Mark where platelets are.
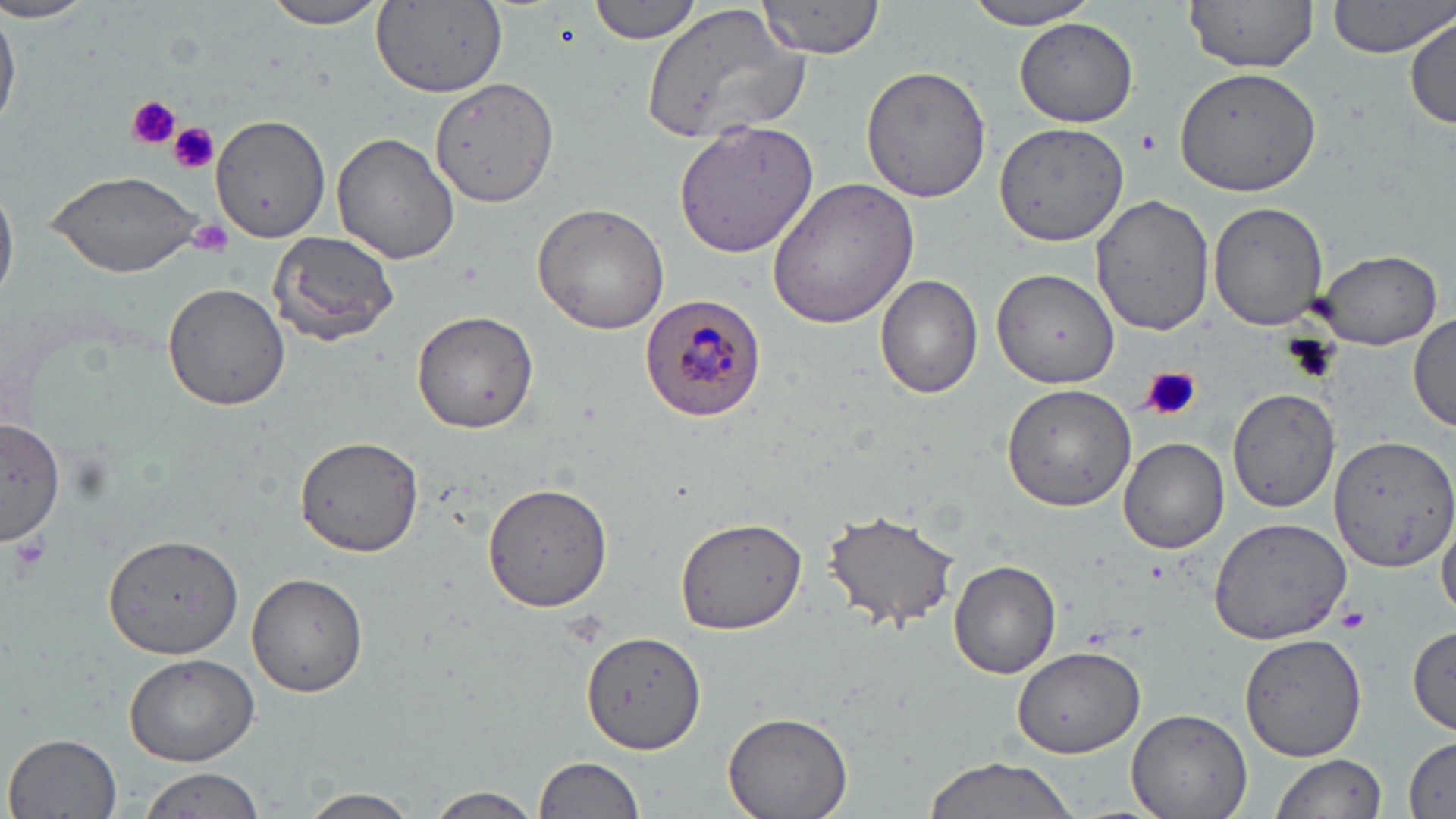
Approximate bounding boxes as named x1/y1/x2/y2 corners in pixels.
Platelets: (x1=124, y1=95, x2=180, y2=151), (x1=169, y1=122, x2=220, y2=174), (x1=1135, y1=128, x2=1162, y2=154), (x1=187, y1=217, x2=235, y2=256), (x1=1141, y1=366, x2=1201, y2=423), (x1=5, y1=534, x2=50, y2=584), (x1=1336, y1=604, x2=1371, y2=635).

{
  "slide_level_diagnosis": "Plasmodium malariae",
  "magnification": "1000x",
  "modality": "light microscopy",
  "preparation": "thin blood smear",
  "image_size": "1456×819 pixels",
  "uninfected_red_blood_cell_locations": "approximate bounding boxes as named x1/y1/x2/y2 corners in pixels: (x1=588, y1=0, x2=705, y2=44), (x1=1184, y1=0, x2=1320, y2=71), (x1=1327, y1=0, x2=1455, y2=59), (x1=963, y1=1, x2=1105, y2=28), (x1=0, y1=2, x2=98, y2=25), (x1=257, y1=2, x2=394, y2=29), (x1=373, y1=2, x2=510, y2=97), (x1=756, y1=2, x2=887, y2=58), (x1=0, y1=3, x2=19, y2=134), (x1=642, y1=4, x2=811, y2=145), (x1=1408, y1=13, x2=1455, y2=130), (x1=1014, y1=17, x2=1139, y2=127), (x1=860, y1=63, x2=991, y2=203), (x1=1172, y1=64, x2=1323, y2=196), (x1=432, y1=76, x2=559, y2=208), (x1=210, y1=112, x2=331, y2=243), (x1=674, y1=116, x2=821, y2=259), (x1=996, y1=120, x2=1131, y2=251), (x1=330, y1=131, x2=462, y2=265), (x1=45, y1=169, x2=206, y2=277), (x1=765, y1=176, x2=922, y2=330), (x1=0, y1=178, x2=18, y2=307), (x1=290, y1=183, x2=439, y2=335), (x1=1092, y1=194, x2=1215, y2=335), (x1=1208, y1=201, x2=1329, y2=330), (x1=531, y1=203, x2=670, y2=335), (x1=268, y1=230, x2=402, y2=346), (x1=1312, y1=248, x2=1442, y2=350), (x1=991, y1=267, x2=1119, y2=390), (x1=876, y1=275, x2=984, y2=400), (x1=161, y1=283, x2=291, y2=411), (x1=410, y1=310, x2=539, y2=433), (x1=1410, y1=312, x2=1456, y2=434), (x1=1000, y1=383, x2=1137, y2=511), (x1=1228, y1=387, x2=1342, y2=512), (x1=1, y1=417, x2=64, y2=546), (x1=295, y1=435, x2=422, y2=557), (x1=1329, y1=435, x2=1456, y2=573), (x1=1119, y1=436, x2=1229, y2=554), (x1=482, y1=481, x2=617, y2=611), (x1=822, y1=508, x2=961, y2=633), (x1=1437, y1=511, x2=1456, y2=619), (x1=675, y1=517, x2=806, y2=635), (x1=1208, y1=517, x2=1349, y2=645), (x1=108, y1=524, x2=244, y2=700), (x1=950, y1=560, x2=1061, y2=679), (x1=245, y1=571, x2=368, y2=697), (x1=1407, y1=624, x2=1454, y2=735), (x1=583, y1=629, x2=707, y2=753), (x1=1238, y1=632, x2=1368, y2=763), (x1=1012, y1=646, x2=1145, y2=757), (x1=123, y1=652, x2=258, y2=766), (x1=1126, y1=708, x2=1253, y2=819), (x1=722, y1=709, x2=855, y2=819), (x1=5, y1=731, x2=124, y2=819), (x1=1403, y1=737, x2=1455, y2=816), (x1=1271, y1=752, x2=1387, y2=819), (x1=535, y1=754, x2=647, y2=819), (x1=921, y1=755, x2=1081, y2=819), (x1=136, y1=767, x2=266, y2=819), (x1=423, y1=786, x2=541, y2=819), (x1=296, y1=788, x2=422, y2=819)",
  "plasmodium_malariae_infected_red_blood_cell_locations": "approximate bounding boxes as named x1/y1/x2/y2 corners in pixels: (x1=635, y1=294, x2=768, y2=424)",
  "stain": "May-Grünwald-Giemsa",
  "field_of_view": "single"
}